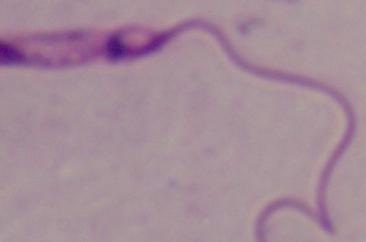 Photomicrograph. Captured at 1000x magnification. A Leishmania parasite is shown.